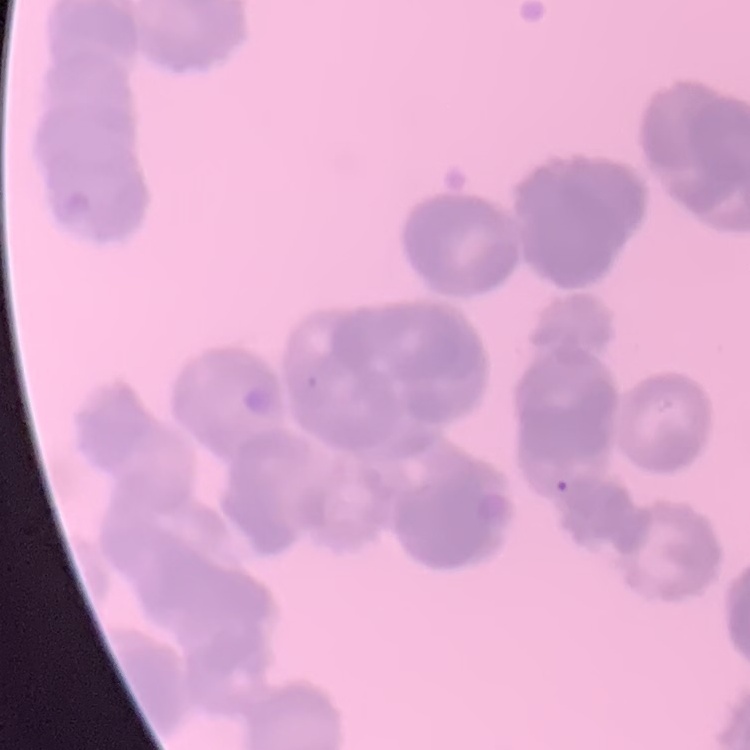

erythrocyte morphology = rouleaux formation
image type = one tile cut from a larger photomicrograph
stain = Field's or Giemsa
preparation = thin peripheral smear